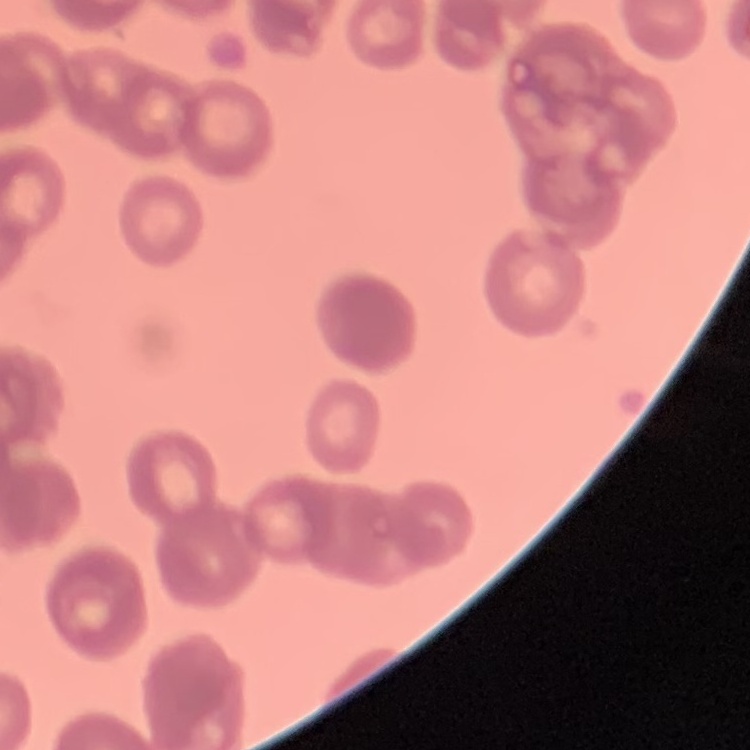

The erythrocytes show rouleaux formation. One tile cut from a larger photomicrograph. Thin blood smear. Field's or Giemsa stain.